Locate every blood parasite and identify its species.
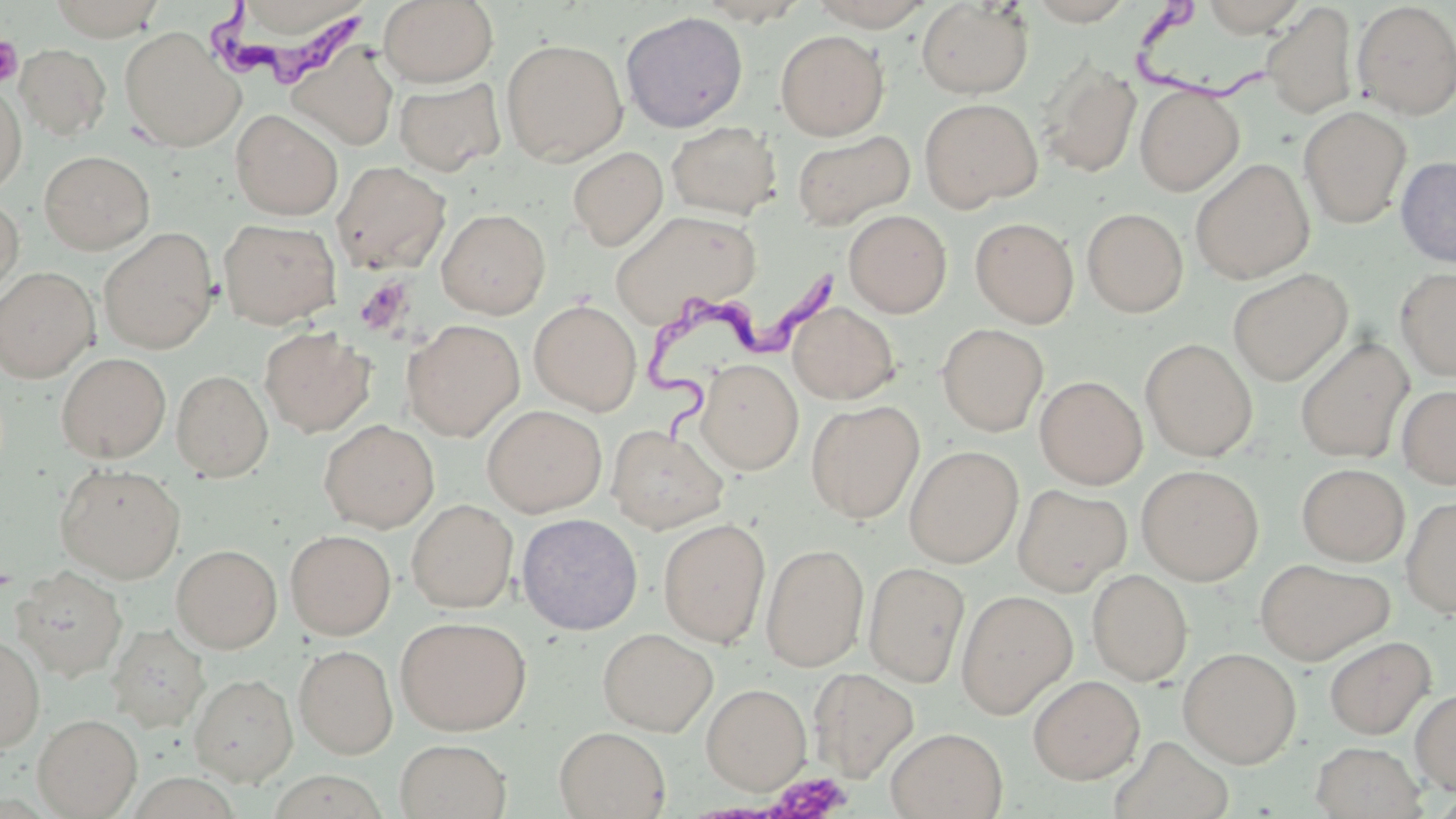

Approximate bounding boxes as named x1/y1/x2/y2 corners in pixels.
Trypanosoma brucei: (x1=208, y1=1, x2=373, y2=92), (x1=1130, y1=3, x2=1268, y2=103), (x1=643, y1=255, x2=842, y2=447).
No Plasmodium falciparum, Plasmodium ovale, Plasmodium malariae, Plasmodium vivax, or Babesia divergens observed.

slide-level diagnosis = Trypanosoma brucei
field of view = one of a larger specimen
magnification = 1000x
preparation = thin blood smear
image size = 1456×819 pixels
modality = optical microscopy
platelet locations = approximate bounding boxes as named x1/y1/x2/y2 corners in pixels: (x1=0, y1=35, x2=24, y2=87), (x1=354, y1=277, x2=413, y2=335), (x1=767, y1=773, x2=852, y2=818)
uninfected red blood cell locations = approximate bounding boxes as named x1/y1/x2/y2 corners in pixels: (x1=46, y1=0, x2=170, y2=39), (x1=379, y1=0, x2=498, y2=86), (x1=806, y1=0, x2=937, y2=30), (x1=916, y1=1, x2=1034, y2=98), (x1=1352, y1=2, x2=1456, y2=119), (x1=1260, y1=4, x2=1358, y2=120), (x1=620, y1=11, x2=749, y2=132), (x1=119, y1=28, x2=243, y2=151), (x1=775, y1=30, x2=888, y2=139), (x1=500, y1=38, x2=628, y2=166), (x1=16, y1=43, x2=111, y2=141), (x1=287, y1=47, x2=400, y2=151), (x1=1038, y1=59, x2=1141, y2=179), (x1=394, y1=78, x2=506, y2=175), (x1=0, y1=80, x2=27, y2=195), (x1=1135, y1=85, x2=1244, y2=195), (x1=920, y1=98, x2=1042, y2=211), (x1=1299, y1=106, x2=1412, y2=228), (x1=230, y1=109, x2=343, y2=219), (x1=667, y1=121, x2=782, y2=220), (x1=791, y1=129, x2=915, y2=230), (x1=569, y1=146, x2=668, y2=250), (x1=39, y1=150, x2=155, y2=254), (x1=1396, y1=156, x2=1456, y2=267), (x1=1190, y1=158, x2=1315, y2=283), (x1=332, y1=160, x2=451, y2=274), (x1=0, y1=195, x2=24, y2=302), (x1=1082, y1=207, x2=1189, y2=318), (x1=436, y1=208, x2=550, y2=318), (x1=608, y1=208, x2=763, y2=326), (x1=844, y1=209, x2=952, y2=317), (x1=970, y1=216, x2=1079, y2=328), (x1=219, y1=218, x2=341, y2=328), (x1=98, y1=228, x2=218, y2=353), (x1=0, y1=267, x2=98, y2=381), (x1=1228, y1=268, x2=1353, y2=385), (x1=1395, y1=268, x2=1456, y2=380), (x1=529, y1=300, x2=641, y2=414), (x1=787, y1=302, x2=900, y2=404), (x1=402, y1=319, x2=523, y2=440), (x1=937, y1=323, x2=1049, y2=435), (x1=259, y1=326, x2=376, y2=437), (x1=1295, y1=337, x2=1414, y2=463), (x1=1141, y1=338, x2=1257, y2=461), (x1=57, y1=352, x2=171, y2=462), (x1=696, y1=359, x2=803, y2=474), (x1=171, y1=369, x2=273, y2=481), (x1=1035, y1=376, x2=1147, y2=488), (x1=1397, y1=385, x2=1456, y2=489), (x1=806, y1=400, x2=925, y2=523), (x1=482, y1=405, x2=606, y2=517), (x1=319, y1=419, x2=439, y2=532), (x1=606, y1=424, x2=729, y2=533), (x1=904, y1=445, x2=1023, y2=568), (x1=1297, y1=463, x2=1409, y2=566), (x1=55, y1=464, x2=186, y2=582), (x1=1137, y1=464, x2=1264, y2=584), (x1=1013, y1=484, x2=1132, y2=595), (x1=1400, y1=496, x2=1456, y2=617), (x1=406, y1=499, x2=518, y2=613), (x1=517, y1=513, x2=643, y2=634), (x1=658, y1=518, x2=770, y2=647), (x1=285, y1=529, x2=396, y2=640), (x1=761, y1=543, x2=869, y2=672), (x1=171, y1=544, x2=282, y2=653), (x1=1254, y1=557, x2=1397, y2=664), (x1=863, y1=561, x2=970, y2=687), (x1=12, y1=566, x2=127, y2=681), (x1=1087, y1=569, x2=1192, y2=685), (x1=956, y1=588, x2=1077, y2=718), (x1=395, y1=615, x2=531, y2=735), (x1=107, y1=623, x2=211, y2=733), (x1=598, y1=627, x2=718, y2=736), (x1=0, y1=633, x2=45, y2=752), (x1=1324, y1=636, x2=1435, y2=738), (x1=294, y1=645, x2=397, y2=758), (x1=1179, y1=647, x2=1301, y2=767), (x1=808, y1=666, x2=919, y2=782), (x1=190, y1=673, x2=298, y2=786), (x1=1028, y1=675, x2=1144, y2=783), (x1=702, y1=683, x2=811, y2=794), (x1=1411, y1=688, x2=1456, y2=795), (x1=33, y1=713, x2=143, y2=818), (x1=554, y1=726, x2=671, y2=818), (x1=885, y1=726, x2=1008, y2=818), (x1=1112, y1=736, x2=1235, y2=819), (x1=394, y1=738, x2=512, y2=818), (x1=1310, y1=740, x2=1428, y2=819)
stain = May-Grünwald-Giemsa